Locate every Plasmodium vivax-infected red blood cell.
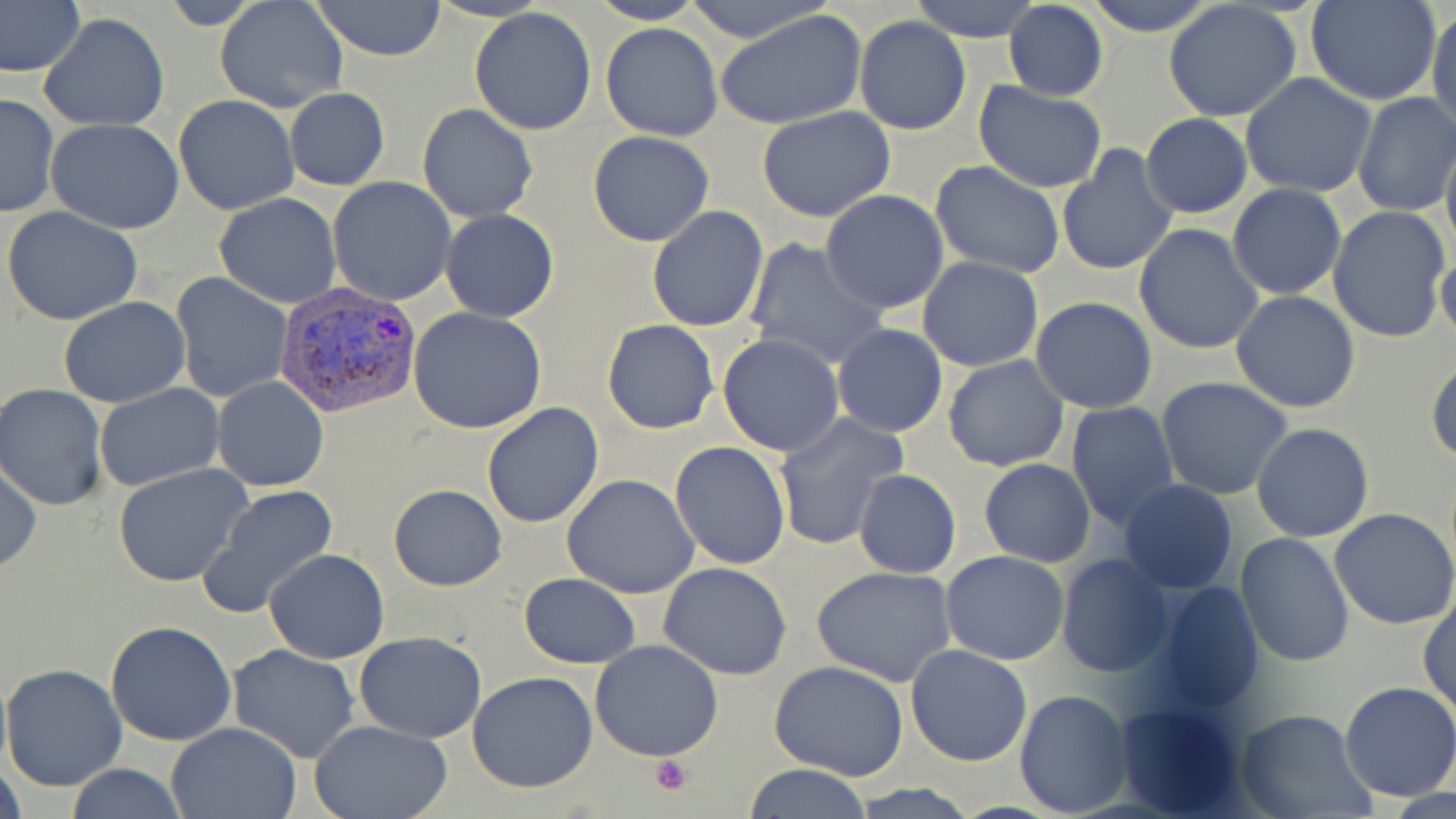
Approximate bounding boxes as (x1, y1, x2, y2) in pixels.
Plasmodium vivax-infected red blood cells: (275, 280, 418, 417).

slide-level diagnosis = Plasmodium vivax
stain = May-Grünwald-Giemsa
magnification = 1000x
image size = 1456×819 pixels
platelet locations = approximate bounding boxes as (x1, y1, x2, y2) in pixels: (649, 754, 694, 795)
preparation = thin blood film
modality = optical microscopy
uninfected red blood cell locations = approximate bounding boxes as (x1, y1, x2, y2) in pixels: (155, 0, 269, 30), (309, 0, 446, 60), (587, 0, 707, 24), (680, 0, 834, 44), (1079, 0, 1222, 37), (1305, 0, 1442, 104), (214, 1, 347, 114), (908, 1, 1043, 41), (1163, 1, 1303, 123), (0, 2, 83, 77), (1004, 2, 1109, 101), (1428, 6, 1456, 137), (469, 7, 599, 136), (717, 10, 867, 130), (39, 13, 168, 131), (855, 16, 972, 136), (600, 21, 724, 141), (1241, 73, 1376, 198), (974, 83, 1108, 193), (284, 87, 390, 191), (1353, 91, 1456, 218), (0, 92, 60, 219), (174, 94, 298, 214), (417, 103, 539, 222), (758, 105, 895, 223), (961, 106, 1100, 255), (1139, 113, 1253, 219), (46, 119, 186, 235), (587, 130, 714, 247), (1440, 135, 1456, 262), (1056, 146, 1177, 276), (930, 161, 1065, 278), (328, 177, 456, 304), (1227, 184, 1346, 299), (820, 191, 949, 315), (213, 193, 342, 307), (2, 205, 143, 325), (646, 205, 770, 332), (1328, 205, 1452, 344), (441, 209, 560, 323), (1133, 223, 1264, 356), (745, 237, 887, 370), (1436, 250, 1456, 343), (916, 257, 1044, 372), (171, 272, 293, 402), (1231, 291, 1362, 414), (59, 296, 189, 407), (1030, 296, 1157, 414), (409, 306, 548, 434), (602, 318, 720, 434), (831, 323, 948, 437), (718, 334, 845, 456), (942, 355, 1070, 474), (1427, 357, 1456, 465), (213, 375, 328, 492), (1156, 376, 1294, 500), (0, 384, 108, 511), (94, 384, 223, 493), (1064, 402, 1181, 533), (480, 403, 604, 529), (771, 411, 907, 551), (1250, 422, 1374, 543), (670, 440, 790, 572), (977, 457, 1096, 567), (0, 460, 42, 575), (114, 463, 251, 588), (853, 469, 962, 578), (561, 474, 699, 598), (1116, 479, 1239, 595), (199, 485, 338, 618), (388, 485, 506, 592), (1330, 508, 1456, 629), (1235, 531, 1356, 667), (262, 549, 389, 664), (939, 550, 1070, 665), (1057, 553, 1173, 676), (658, 563, 792, 680), (810, 564, 958, 686), (517, 573, 641, 669), (1149, 580, 1264, 715), (1418, 594, 1455, 713), (105, 621, 237, 746), (354, 631, 487, 744), (589, 639, 724, 761), (227, 643, 361, 765), (905, 645, 1033, 767), (769, 660, 908, 782), (1, 661, 127, 792), (467, 672, 598, 793), (1338, 680, 1456, 802), (1014, 689, 1133, 817), (1115, 699, 1249, 817), (1235, 710, 1375, 819), (310, 720, 454, 819), (167, 721, 301, 819), (0, 762, 28, 819), (741, 763, 874, 818), (63, 764, 189, 819), (849, 784, 983, 817)
field of view = single